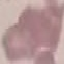
Summary:
  - Malaria status: uninfected
  - Image type: automatically extracted cell patch, resized to 64 × 64 pixels
  - Preparation: thin blood film
  - Stain: Giemsa
  - Capture: smartphone camera at the microscope eyepiece